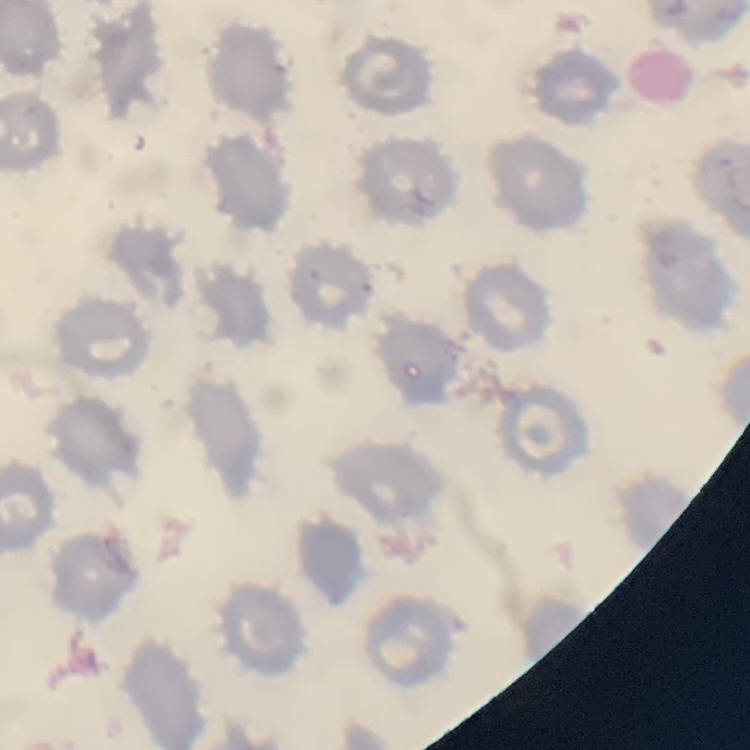
erythrocyte morphology = no rouleaux formation
preparation = thin peripheral smear
stain = Field's or Giemsa
image type = square crop of a larger photomicrograph